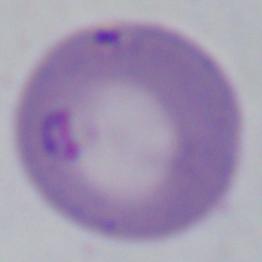

A Babesia parasite is seen. Micrograph. 1000x magnification.